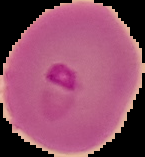

image size = 145×157 pixels
image type = segmented cell region with the area outside set to black
preparation = thin blood smear
malaria status = parasitized